Assess this cell for malaria.
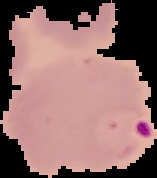

It is parasitized.

image size = 157×178 pixels
preparation = thin blood film
image type = cell region segmented out of the field of view; surrounding area masked to black